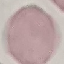

{
  "result": "no malaria parasites seen",
  "preparation": "thin blood film",
  "image_type": "automatically extracted cell patch, resized to 64 × 64 pixels",
  "stain": "Giemsa",
  "capture": "smartphone camera at the microscope eyepiece"
}